Give the extent of all Plasmodium malariae-infected red blood cells.
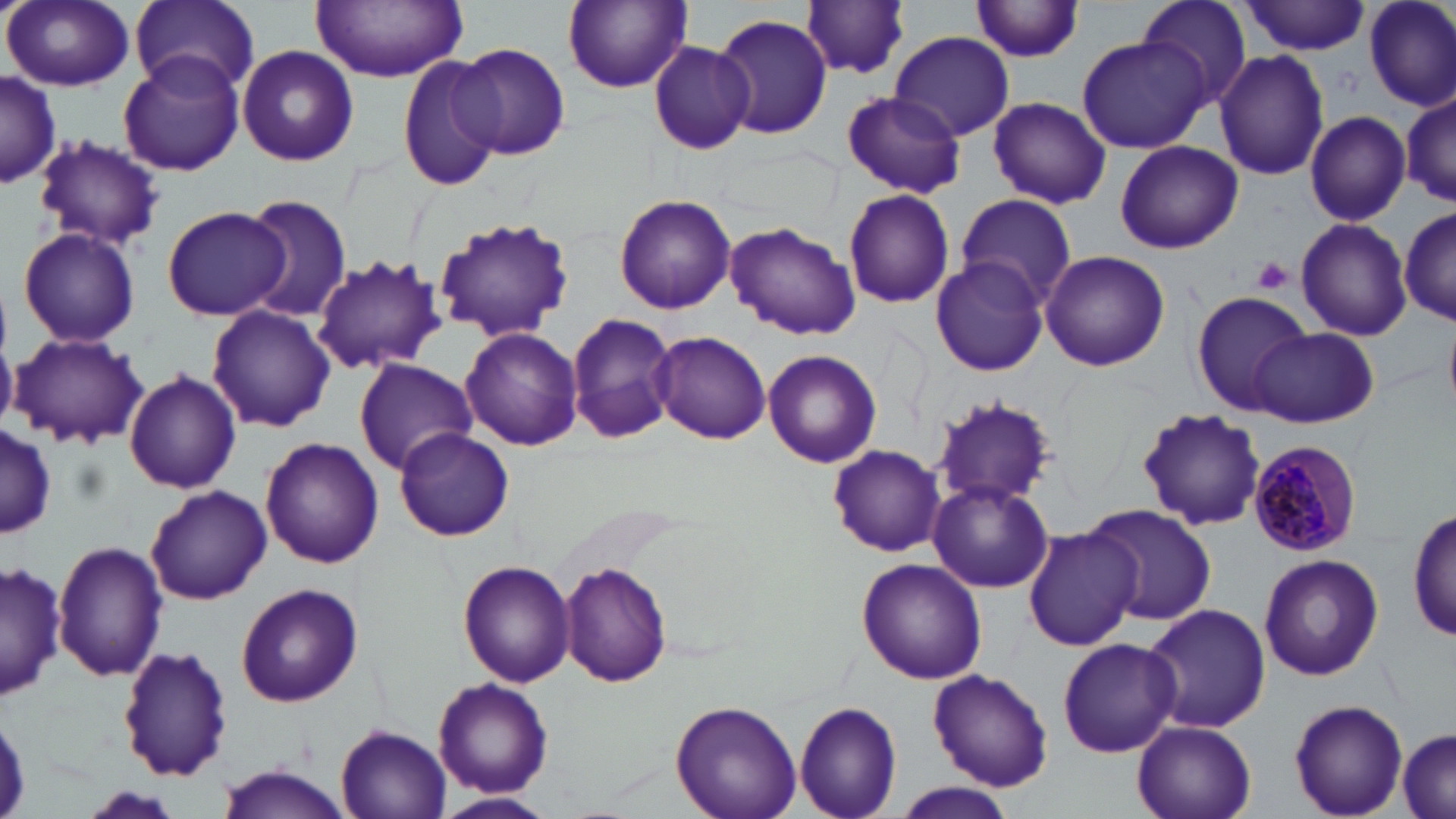

Approximate bounding boxes as [x1, y1, x2, y2] in pixels.
Plasmodium malariae-infected red blood cells: [1248, 440, 1363, 558].

{
  "slide_level_diagnosis": "Plasmodium malariae",
  "uninfected_red_blood_cell_locations": "approximate bounding boxes as [x1, y1, x2, y2] in pixels: [4, 0, 135, 92], [128, 0, 261, 95], [311, 0, 470, 82], [969, 0, 1087, 62], [1134, 0, 1251, 104], [562, 1, 691, 92], [1240, 1, 1370, 55], [1363, 1, 1456, 112], [803, 2, 912, 79], [713, 14, 834, 140], [887, 31, 1016, 141], [1075, 36, 1210, 154], [648, 41, 755, 155], [453, 42, 571, 161], [236, 45, 359, 168], [1213, 48, 1330, 182], [118, 50, 244, 180], [397, 55, 506, 194], [0, 72, 60, 188], [1401, 89, 1455, 208], [841, 90, 966, 198], [986, 97, 1110, 209], [1304, 110, 1411, 224], [32, 136, 163, 252], [1114, 141, 1243, 254], [842, 188, 955, 309], [954, 192, 1077, 308], [614, 193, 736, 315], [241, 195, 354, 323], [161, 206, 292, 321], [1401, 206, 1456, 330], [432, 216, 576, 342], [1295, 217, 1412, 341], [725, 221, 861, 340], [17, 227, 141, 349], [1040, 250, 1170, 372], [312, 253, 446, 375], [931, 253, 1049, 377], [1191, 290, 1315, 416], [207, 304, 336, 432], [567, 314, 675, 443], [1445, 320, 1456, 411], [460, 327, 582, 450], [1251, 327, 1379, 427], [651, 330, 771, 445], [9, 332, 149, 449], [763, 349, 883, 469], [352, 358, 479, 476], [124, 369, 242, 495], [927, 395, 1057, 511], [1137, 408, 1267, 532], [0, 422, 55, 543], [394, 426, 514, 541], [260, 437, 383, 569], [828, 443, 946, 556], [927, 479, 1054, 593], [145, 484, 270, 605], [1085, 503, 1216, 626], [1410, 506, 1455, 647], [884, 511, 1006, 653], [1024, 525, 1140, 651], [53, 537, 170, 683], [1258, 553, 1384, 682], [858, 558, 986, 683], [459, 559, 576, 687], [1, 561, 66, 702], [558, 561, 672, 686], [234, 583, 362, 707], [1140, 602, 1271, 732], [1056, 636, 1182, 758], [117, 644, 231, 782], [927, 669, 1053, 791], [433, 678, 554, 798], [1289, 698, 1408, 818], [669, 700, 803, 819], [793, 701, 902, 819], [1133, 719, 1257, 819], [334, 722, 452, 818], [1396, 726, 1456, 819], [213, 766, 355, 818], [894, 783, 1016, 818], [435, 791, 556, 818]",
  "preparation": "thin blood smear",
  "image_size": "1456×819 pixels",
  "platelet_locations": "approximate bounding boxes as [x1, y1, x2, y2] in pixels: [1252, 257, 1294, 295]",
  "modality": "optical microscopy",
  "stain": "May-Grünwald-Giemsa",
  "field_of_view": "single",
  "magnification": "1000x"
}